Locate and identify every blood parasite.
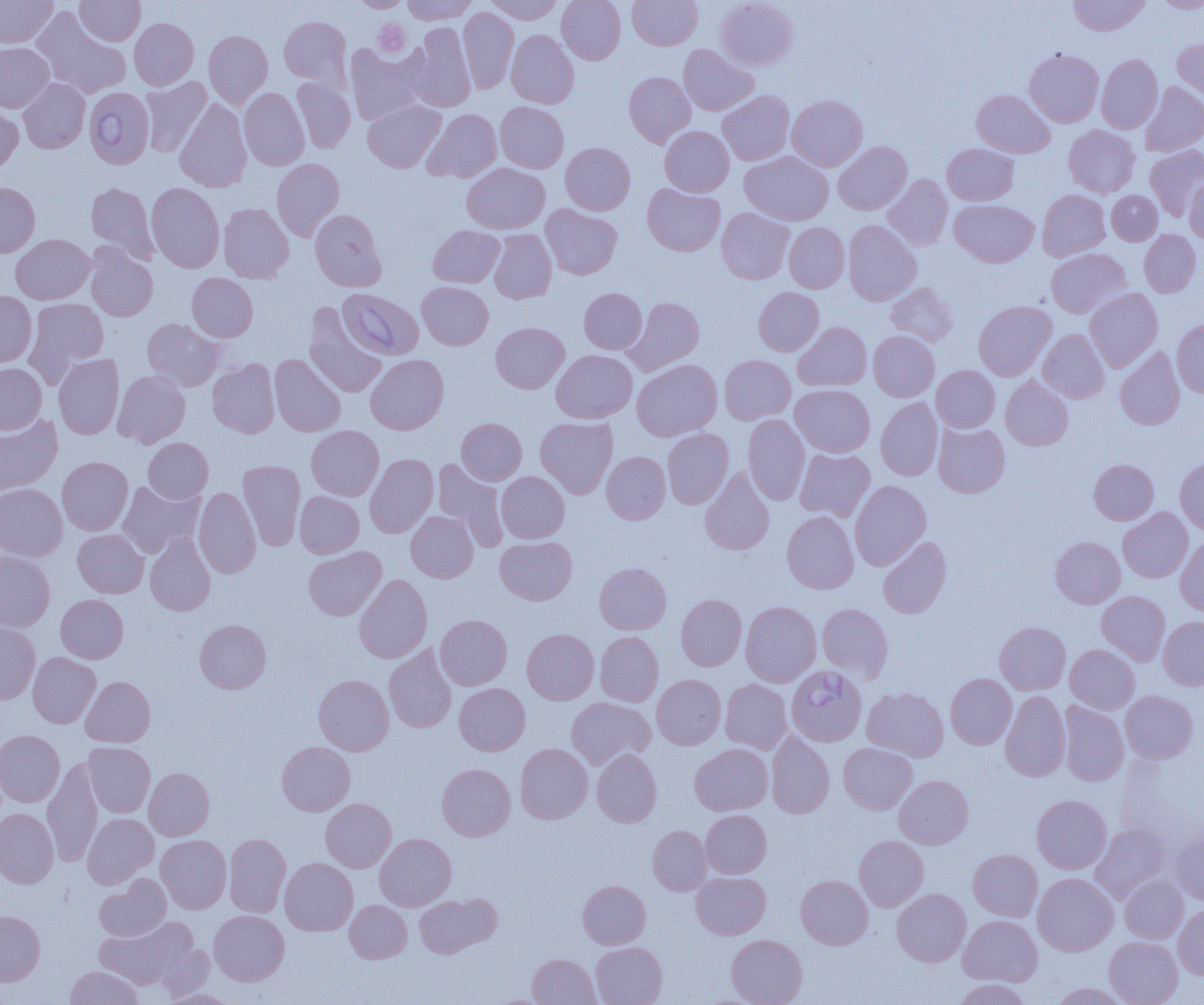

Approximate bounding boxes as named x1/y1/x2/y2 corners in pixels.
Babesia divergens-infected red blood cells: (x1=84, y1=87, x2=154, y2=168), (x1=337, y1=288, x2=423, y2=359), (x1=786, y1=666, x2=866, y2=746).
No Plasmodium falciparum, Plasmodium ovale, Plasmodium malariae, Plasmodium vivax, or Trypanosoma brucei observed.

slide_level_diagnosis: Babesia divergens
uninfected_red_blood_cell_locations: 'approximate bounding boxes as named x1/y1/x2/y2 corners in pixels: (x1=0, y1=0, x2=58, y2=47), (x1=75, y1=0, x2=145, y2=45), (x1=353, y1=0, x2=410, y2=12), (x1=402, y1=0, x2=477, y2=24), (x1=486, y1=0, x2=563, y2=24), (x1=557, y1=0, x2=625, y2=64), (x1=627, y1=0, x2=702, y2=50), (x1=716, y1=0, x2=799, y2=71), (x1=1068, y1=0, x2=1150, y2=36), (x1=1154, y1=0, x2=1204, y2=13), (x1=458, y1=7, x2=519, y2=94), (x1=32, y1=8, x2=132, y2=99), (x1=279, y1=16, x2=352, y2=88), (x1=129, y1=18, x2=198, y2=89), (x1=407, y1=22, x2=476, y2=112), (x1=204, y1=30, x2=273, y2=108), (x1=507, y1=30, x2=579, y2=108), (x1=1172, y1=37, x2=1204, y2=106), (x1=0, y1=42, x2=54, y2=112), (x1=345, y1=43, x2=427, y2=125), (x1=678, y1=44, x2=758, y2=116), (x1=1024, y1=49, x2=1104, y2=127), (x1=1096, y1=54, x2=1163, y2=134), (x1=624, y1=71, x2=695, y2=147), (x1=141, y1=77, x2=211, y2=156), (x1=292, y1=77, x2=355, y2=153), (x1=18, y1=78, x2=90, y2=153), (x1=1140, y1=81, x2=1204, y2=157), (x1=239, y1=88, x2=309, y2=170), (x1=717, y1=90, x2=794, y2=165), (x1=972, y1=90, x2=1055, y2=158), (x1=787, y1=95, x2=867, y2=171), (x1=175, y1=99, x2=251, y2=192), (x1=363, y1=99, x2=445, y2=172), (x1=495, y1=101, x2=569, y2=173), (x1=0, y1=103, x2=23, y2=174), (x1=422, y1=109, x2=501, y2=182), (x1=1064, y1=125, x2=1140, y2=197), (x1=660, y1=126, x2=734, y2=196), (x1=833, y1=142, x2=912, y2=215), (x1=560, y1=143, x2=635, y2=215), (x1=943, y1=143, x2=1018, y2=205), (x1=1146, y1=145, x2=1204, y2=220), (x1=740, y1=152, x2=833, y2=225), (x1=272, y1=158, x2=345, y2=241), (x1=462, y1=164, x2=550, y2=234), (x1=1184, y1=174, x2=1204, y2=244), (x1=883, y1=175, x2=952, y2=250), (x1=0, y1=182, x2=40, y2=258), (x1=86, y1=182, x2=157, y2=262), (x1=146, y1=182, x2=224, y2=273), (x1=642, y1=183, x2=725, y2=256), (x1=1038, y1=189, x2=1110, y2=260), (x1=1107, y1=190, x2=1162, y2=245), (x1=950, y1=199, x2=1039, y2=267), (x1=218, y1=203, x2=294, y2=283), (x1=541, y1=204, x2=622, y2=279), (x1=716, y1=208, x2=794, y2=284), (x1=310, y1=209, x2=387, y2=291), (x1=843, y1=220, x2=921, y2=305), (x1=784, y1=222, x2=850, y2=293), (x1=428, y1=225, x2=504, y2=287), (x1=489, y1=229, x2=556, y2=303), (x1=1139, y1=229, x2=1201, y2=297), (x1=11, y1=234, x2=95, y2=304), (x1=85, y1=243, x2=158, y2=321), (x1=1046, y1=248, x2=1130, y2=318), (x1=187, y1=273, x2=258, y2=342), (x1=417, y1=281, x2=493, y2=350), (x1=885, y1=282, x2=958, y2=346), (x1=754, y1=287, x2=824, y2=356), (x1=579, y1=288, x2=647, y2=354), (x1=1085, y1=288, x2=1162, y2=371), (x1=0, y1=291, x2=37, y2=368), (x1=624, y1=297, x2=704, y2=375), (x1=24, y1=298, x2=109, y2=383), (x1=974, y1=301, x2=1056, y2=381), (x1=303, y1=303, x2=387, y2=397), (x1=142, y1=318, x2=225, y2=391), (x1=1172, y1=319, x2=1204, y2=397), (x1=491, y1=322, x2=569, y2=393), (x1=793, y1=322, x2=871, y2=391), (x1=1038, y1=329, x2=1109, y2=403), (x1=868, y1=331, x2=939, y2=401), (x1=1115, y1=347, x2=1185, y2=430), (x1=551, y1=349, x2=637, y2=423), (x1=54, y1=354, x2=124, y2=439), (x1=270, y1=354, x2=346, y2=437), (x1=365, y1=354, x2=449, y2=434), (x1=719, y1=355, x2=795, y2=425), (x1=208, y1=358, x2=280, y2=437), (x1=632, y1=359, x2=722, y2=441), (x1=0, y1=363, x2=46, y2=435), (x1=932, y1=365, x2=999, y2=432), (x1=113, y1=370, x2=190, y2=448), (x1=1001, y1=376, x2=1073, y2=450), (x1=790, y1=384, x2=875, y2=457), (x1=876, y1=398, x2=943, y2=480), (x1=743, y1=414, x2=810, y2=504), (x1=0, y1=415, x2=62, y2=495), (x1=535, y1=417, x2=618, y2=499), (x1=456, y1=418, x2=527, y2=485), (x1=933, y1=422, x2=1010, y2=497), (x1=306, y1=425, x2=384, y2=500), (x1=662, y1=428, x2=733, y2=509), (x1=143, y1=438, x2=213, y2=503), (x1=795, y1=449, x2=875, y2=521), (x1=602, y1=451, x2=670, y2=524), (x1=365, y1=453, x2=438, y2=538), (x1=57, y1=457, x2=133, y2=535), (x1=1175, y1=458, x2=1204, y2=534), (x1=432, y1=459, x2=508, y2=551), (x1=1089, y1=459, x2=1158, y2=525), (x1=238, y1=460, x2=305, y2=550), (x1=700, y1=468, x2=775, y2=555), (x1=496, y1=471, x2=570, y2=543), (x1=850, y1=480, x2=931, y2=570), (x1=117, y1=481, x2=203, y2=558), (x1=0, y1=483, x2=67, y2=561), (x1=194, y1=487, x2=261, y2=578), (x1=295, y1=491, x2=364, y2=558), (x1=1118, y1=508, x2=1193, y2=583), (x1=406, y1=511, x2=478, y2=582), (x1=782, y1=511, x2=858, y2=593), (x1=73, y1=529, x2=149, y2=598), (x1=145, y1=532, x2=216, y2=616), (x1=495, y1=536, x2=577, y2=605), (x1=878, y1=537, x2=951, y2=618), (x1=1051, y1=537, x2=1125, y2=608), (x1=1176, y1=538, x2=1204, y2=616), (x1=304, y1=546, x2=386, y2=620), (x1=0, y1=551, x2=55, y2=632), (x1=595, y1=562, x2=671, y2=634), (x1=354, y1=574, x2=432, y2=663), (x1=1097, y1=591, x2=1170, y2=665), (x1=56, y1=594, x2=128, y2=663), (x1=676, y1=594, x2=747, y2=670), (x1=740, y1=601, x2=821, y2=686), (x1=817, y1=604, x2=893, y2=682), (x1=435, y1=614, x2=512, y2=690), (x1=1158, y1=616, x2=1204, y2=690), (x1=194, y1=619, x2=271, y2=693), (x1=0, y1=621, x2=40, y2=705), (x1=995, y1=622, x2=1070, y2=694), (x1=522, y1=629, x2=599, y2=704), (x1=595, y1=631, x2=663, y2=706), (x1=384, y1=644, x2=457, y2=733), (x1=1065, y1=645, x2=1139, y2=713), (x1=28, y1=652, x2=100, y2=728), (x1=946, y1=673, x2=1016, y2=749), (x1=652, y1=674, x2=726, y2=749), (x1=313, y1=675, x2=394, y2=755), (x1=81, y1=676, x2=156, y2=747), (x1=720, y1=679, x2=792, y2=754), (x1=454, y1=683, x2=530, y2=755), (x1=862, y1=687, x2=949, y2=761), (x1=1120, y1=690, x2=1198, y2=763), (x1=1000, y1=691, x2=1070, y2=781), (x1=566, y1=697, x2=655, y2=769), (x1=1058, y1=701, x2=1129, y2=786), (x1=0, y1=730, x2=65, y2=807), (x1=766, y1=732, x2=834, y2=818), (x1=277, y1=741, x2=355, y2=816), (x1=82, y1=742, x2=155, y2=817), (x1=838, y1=742, x2=917, y2=814), (x1=515, y1=744, x2=593, y2=823), (x1=690, y1=744, x2=772, y2=815), (x1=592, y1=749, x2=662, y2=827), (x1=42, y1=759, x2=103, y2=867), (x1=437, y1=763, x2=516, y2=841), (x1=144, y1=767, x2=214, y2=841), (x1=894, y1=775, x2=973, y2=849), (x1=1032, y1=795, x2=1112, y2=874), (x1=320, y1=798, x2=396, y2=872), (x1=0, y1=808, x2=58, y2=888), (x1=700, y1=810, x2=772, y2=878), (x1=82, y1=813, x2=158, y2=888), (x1=1090, y1=824, x2=1170, y2=902), (x1=647, y1=825, x2=712, y2=895), (x1=1171, y1=825, x2=1204, y2=905), (x1=224, y1=833, x2=291, y2=917), (x1=375, y1=833, x2=456, y2=910), (x1=156, y1=835, x2=231, y2=913), (x1=855, y1=835, x2=928, y2=910), (x1=968, y1=849, x2=1043, y2=921), (x1=280, y1=858, x2=358, y2=935), (x1=691, y1=872, x2=770, y2=939), (x1=1032, y1=873, x2=1118, y2=955), (x1=95, y1=874, x2=171, y2=941), (x1=796, y1=875, x2=873, y2=949), (x1=1120, y1=875, x2=1188, y2=944), (x1=578, y1=880, x2=651, y2=948), (x1=892, y1=889, x2=971, y2=967), (x1=414, y1=893, x2=500, y2=957), (x1=345, y1=900, x2=412, y2=963), (x1=1173, y1=904, x2=1204, y2=979), (x1=209, y1=910, x2=289, y2=986), (x1=0, y1=911, x2=45, y2=986), (x1=958, y1=915, x2=1042, y2=986), (x1=95, y1=917, x2=198, y2=990), (x1=727, y1=934, x2=808, y2=1005), (x1=1104, y1=936, x2=1182, y2=1005), (x1=590, y1=942, x2=667, y2=1005), (x1=527, y1=953, x2=601, y2=1005), (x1=65, y1=966, x2=143, y2=1004), (x1=953, y1=978, x2=1029, y2=1005), (x1=1052, y1=982, x2=1129, y2=1005), (x1=160, y1=988, x2=235, y2=1004)'
preparation: thin blood smear
platelet_locations: 'approximate bounding boxes as named x1/y1/x2/y2 corners in pixels: (x1=371, y1=18, x2=411, y2=59)'
field_of_view: one of a larger specimen
image_size: 1204×1005 pixels
magnification: 1000x
modality: light microscopy